Report the malaria status of this cell.
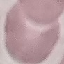

It is uninfected.

Thin smear of blood. Giemsa-stained preparation. Photographed with a smartphone camera at the microscope eyepiece. Automatically extracted cell patch, resized to 64 × 64 pixels.